Identify the parasite.
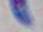

Toxoplasma gondii.

{
  "modality": "photomicrograph",
  "magnification": "1000x"
}